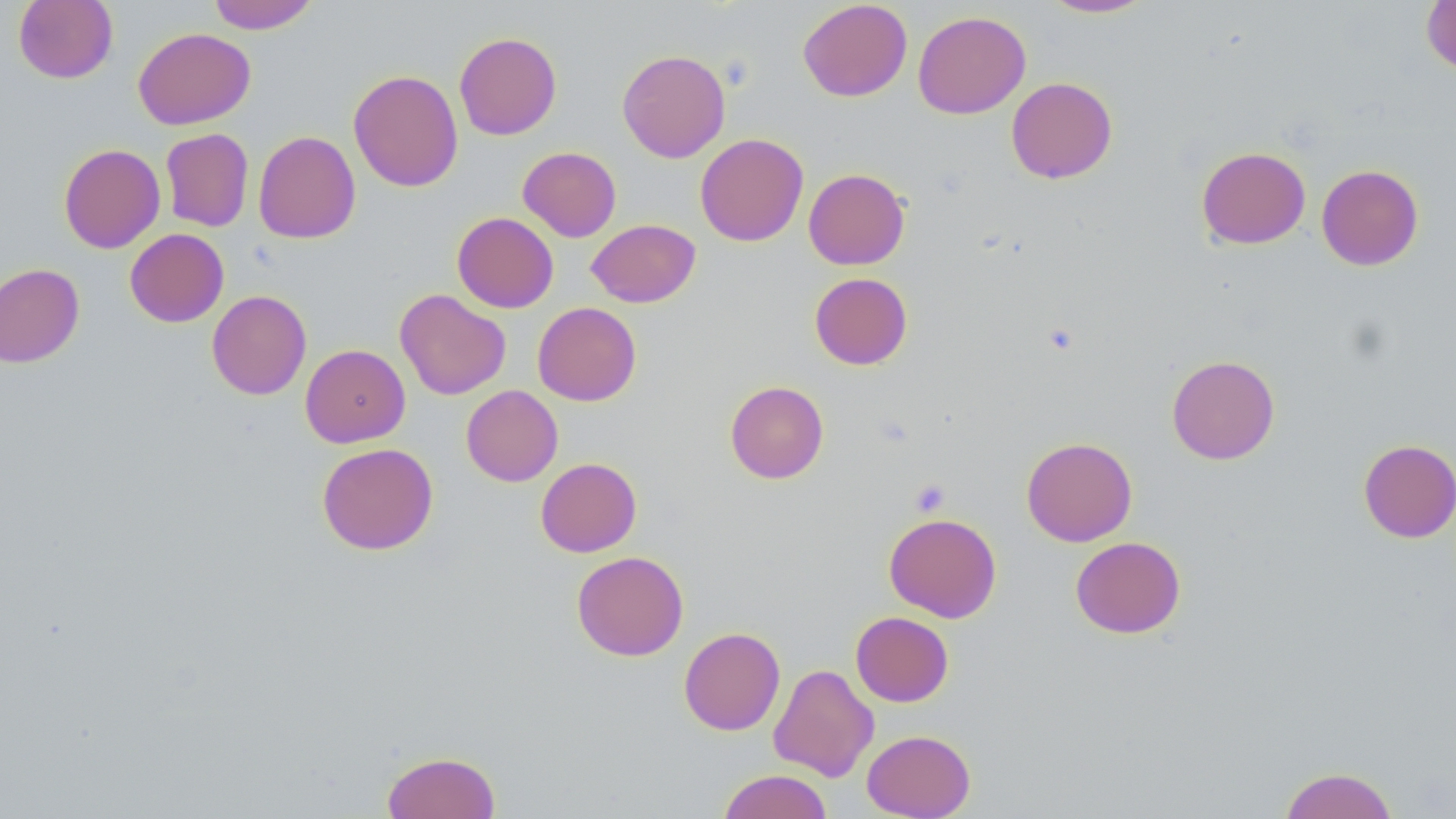
slide-level diagnosis = no evidence of blood parasites
stain = May-Grünwald-Giemsa
image size = 1456×819 pixels
modality = light microscopy
platelet locations = approximate bounding boxes as named x1/y1/x2/y2 corners in pixels: (x1=910, y1=478, x2=951, y2=517)
field of view = one of a larger specimen
preparation = thin blood smear
magnification = 1000x
uninfected red blood cell locations = approximate bounding boxes as named x1/y1/x2/y2 corners in pixels: (x1=13, y1=0, x2=118, y2=83), (x1=798, y1=0, x2=912, y2=102), (x1=1040, y1=0, x2=1155, y2=18), (x1=1421, y1=0, x2=1456, y2=76), (x1=207, y1=1, x2=319, y2=33), (x1=913, y1=11, x2=1031, y2=119), (x1=133, y1=27, x2=255, y2=129), (x1=454, y1=31, x2=562, y2=140), (x1=617, y1=49, x2=731, y2=162), (x1=348, y1=69, x2=463, y2=192), (x1=1006, y1=77, x2=1118, y2=183), (x1=160, y1=128, x2=254, y2=232), (x1=253, y1=131, x2=361, y2=244), (x1=695, y1=133, x2=809, y2=246), (x1=58, y1=143, x2=165, y2=253), (x1=518, y1=146, x2=621, y2=242), (x1=1196, y1=146, x2=1310, y2=249), (x1=1316, y1=164, x2=1424, y2=271), (x1=803, y1=168, x2=910, y2=270), (x1=452, y1=212, x2=558, y2=313), (x1=586, y1=219, x2=701, y2=308), (x1=125, y1=228, x2=229, y2=327), (x1=0, y1=263, x2=84, y2=368), (x1=809, y1=273, x2=912, y2=370), (x1=395, y1=289, x2=511, y2=400), (x1=207, y1=290, x2=311, y2=400), (x1=533, y1=302, x2=641, y2=406), (x1=300, y1=344, x2=410, y2=448), (x1=1166, y1=354, x2=1280, y2=464), (x1=725, y1=380, x2=829, y2=484), (x1=461, y1=385, x2=563, y2=486), (x1=1021, y1=436, x2=1138, y2=546), (x1=1358, y1=439, x2=1456, y2=543), (x1=316, y1=442, x2=438, y2=555), (x1=535, y1=457, x2=642, y2=557), (x1=883, y1=512, x2=1002, y2=622), (x1=1070, y1=536, x2=1186, y2=638), (x1=572, y1=551, x2=688, y2=661), (x1=850, y1=611, x2=954, y2=707), (x1=679, y1=627, x2=785, y2=735), (x1=768, y1=663, x2=878, y2=782), (x1=861, y1=729, x2=976, y2=819), (x1=382, y1=750, x2=501, y2=818), (x1=1278, y1=766, x2=1399, y2=819), (x1=718, y1=769, x2=833, y2=819)